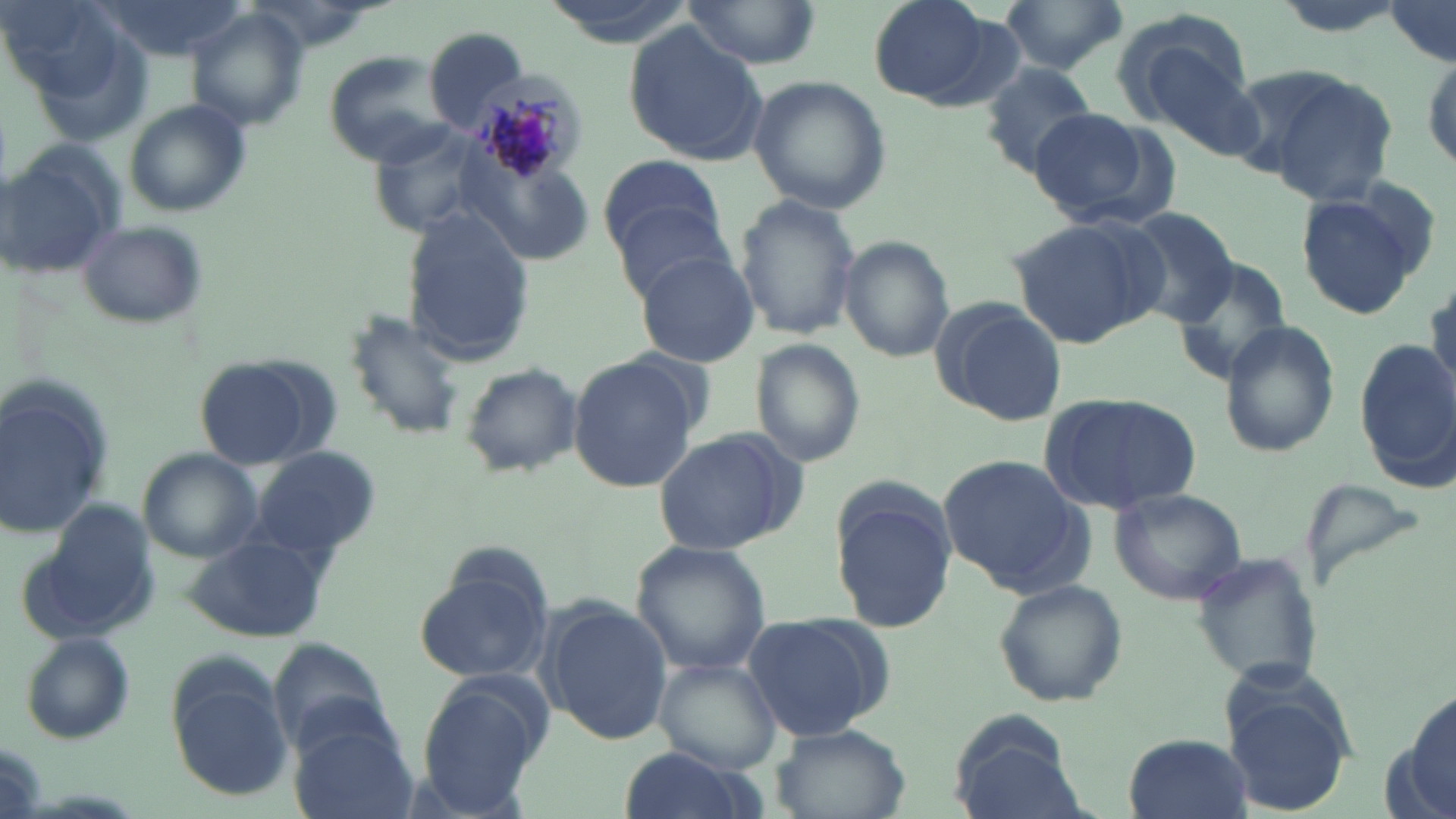

Summary:
  - Coordinate format: approximate bounding boxes as [x1, y1, x2, y2] in pixels
  - Plasmodium malariae-infected red blood cell locations: [469, 66, 585, 187]
  - Uninfected red blood cell locations: [0, 0, 136, 110], [99, 0, 245, 62], [865, 0, 1002, 106], [997, 0, 1130, 73], [683, 1, 818, 68], [1382, 3, 1454, 63], [183, 10, 306, 134], [1117, 19, 1267, 159], [621, 23, 769, 166], [424, 26, 531, 129], [1422, 53, 1455, 175], [324, 54, 459, 164], [981, 63, 1101, 173], [1252, 66, 1401, 204], [749, 75, 890, 215], [124, 101, 252, 217], [1023, 108, 1158, 219], [1, 141, 125, 279], [598, 154, 727, 257], [1293, 187, 1434, 322], [732, 195, 861, 342], [615, 204, 737, 307], [1123, 208, 1240, 323], [1006, 214, 1168, 348], [401, 215, 531, 368], [74, 219, 210, 330], [840, 237, 956, 361], [634, 251, 761, 368], [1171, 257, 1292, 388], [1426, 275, 1456, 399], [930, 299, 1066, 428], [345, 307, 467, 443], [1223, 320, 1340, 458], [749, 339, 868, 468], [1357, 339, 1456, 478], [568, 355, 703, 492], [194, 358, 322, 468], [459, 364, 579, 476], [0, 383, 114, 542], [1038, 392, 1202, 517], [650, 425, 807, 558], [254, 446, 376, 556], [138, 450, 264, 563], [938, 453, 1089, 594], [829, 484, 958, 636], [1108, 485, 1249, 605], [182, 535, 330, 642], [629, 540, 773, 676], [1186, 552, 1325, 689], [412, 563, 552, 683], [992, 578, 1130, 707], [540, 601, 672, 743], [742, 611, 893, 741], [17, 633, 137, 746], [655, 656, 784, 776], [166, 664, 295, 800], [417, 681, 544, 816], [1222, 686, 1357, 816], [1404, 687, 1456, 817], [950, 711, 1084, 818], [290, 720, 419, 819], [769, 724, 909, 818], [1122, 733, 1252, 819], [613, 747, 756, 819]
  - Slide-level diagnosis: Plasmodium malariae
  - Stain: May-Grünwald-Giemsa
  - Modality: light microscopy
  - Magnification: 1000x
  - Preparation: thin blood smear
  - Field of view: one of a larger specimen
  - Image size: 1456×819 pixels